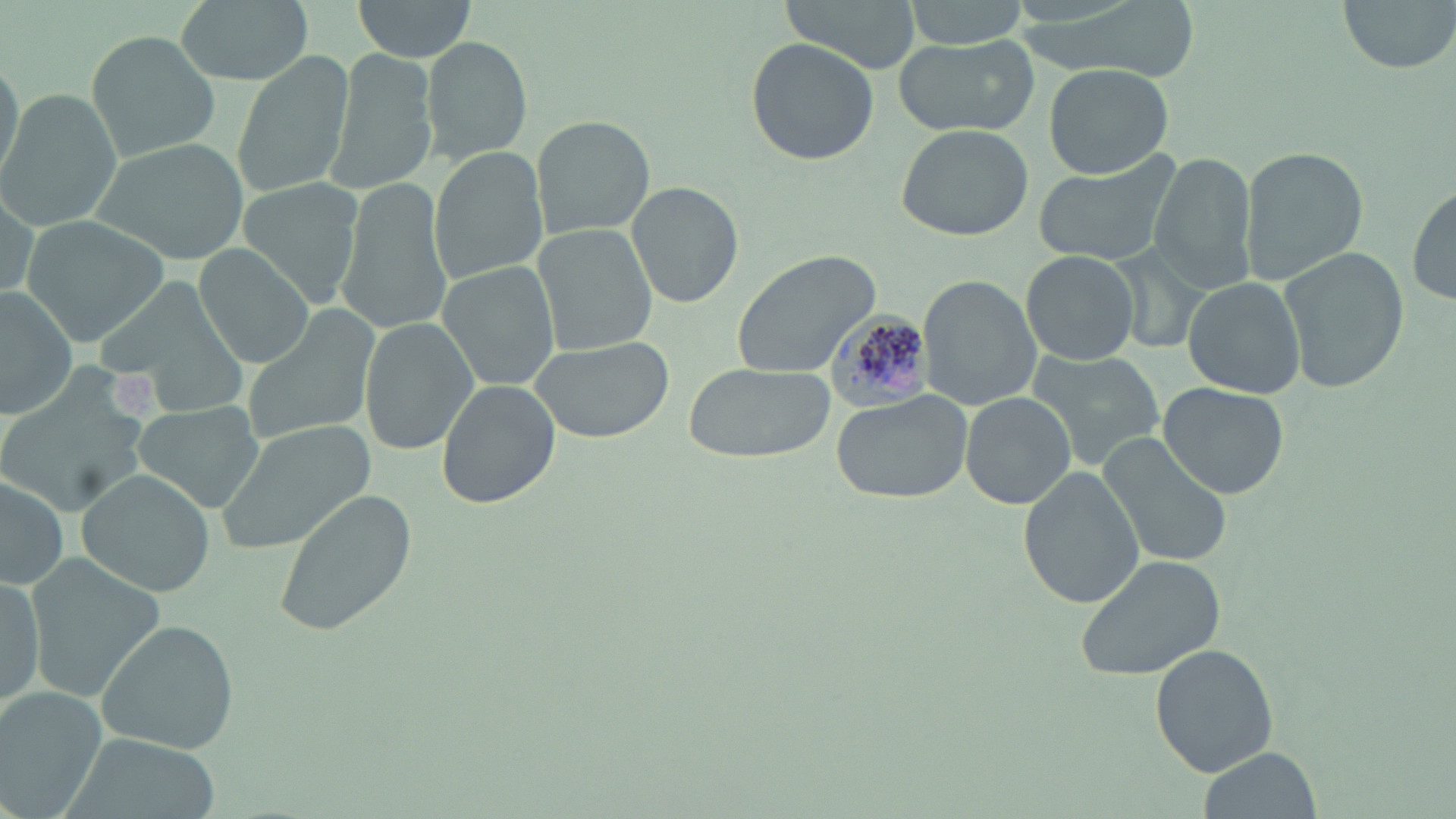

Summary:
  - Coordinate format: approximate bounding boxes as (x1,y1)-(x2,y2) corner pairs in pixels
  - Uninfected red blood cell locations: (172,0)-(316,84), (351,0)-(476,64), (783,0)-(919,72), (899,0)-(1029,49), (1335,0)-(1454,73), (85,30)-(224,164), (421,34)-(532,165), (895,35)-(1037,138), (745,37)-(880,169), (230,50)-(355,199), (329,50)-(437,192), (0,52)-(24,188), (1043,63)-(1174,180), (0,90)-(121,231), (531,114)-(655,243), (896,124)-(1035,240), (93,137)-(248,264), (1238,145)-(1368,284), (427,147)-(548,288), (1032,150)-(1183,268), (1150,153)-(1260,294), (333,174)-(452,340), (237,176)-(368,310), (627,180)-(745,309), (1,184)-(41,305), (1410,184)-(1456,307), (20,215)-(170,346), (531,221)-(659,357), (191,243)-(317,368), (1277,245)-(1406,395), (730,247)-(880,378), (1023,250)-(1138,365), (438,261)-(561,393), (95,274)-(248,416), (917,275)-(1042,412), (1184,276)-(1306,400), (0,288)-(78,419), (241,303)-(381,448), (359,316)-(478,456), (527,335)-(675,444), (1024,347)-(1167,473), (684,360)-(834,465), (0,365)-(154,520), (437,380)-(559,508), (1159,383)-(1289,499), (828,391)-(974,506), (960,393)-(1076,510), (130,401)-(265,513), (217,420)-(377,555), (1097,433)-(1233,568), (1020,465)-(1143,608), (75,469)-(215,595), (0,473)-(71,591), (271,491)-(416,636), (26,552)-(166,700), (1075,553)-(1227,682), (0,568)-(50,709), (98,618)-(242,756), (1150,645)-(1278,774), (0,689)-(103,818), (53,734)-(221,819), (1197,747)-(1321,819)
  - Plasmodium malariae-infected red blood cell locations: (829,312)-(937,415)
  - Slide-level diagnosis: Plasmodium malariae
  - Magnification: 1000x
  - Image size: 1456×819 pixels
  - Stain: May-Grünwald-Giemsa
  - Field of view: one of a larger specimen
  - Preparation: thin blood film
  - Modality: optical microscopy